Give the preparation type.
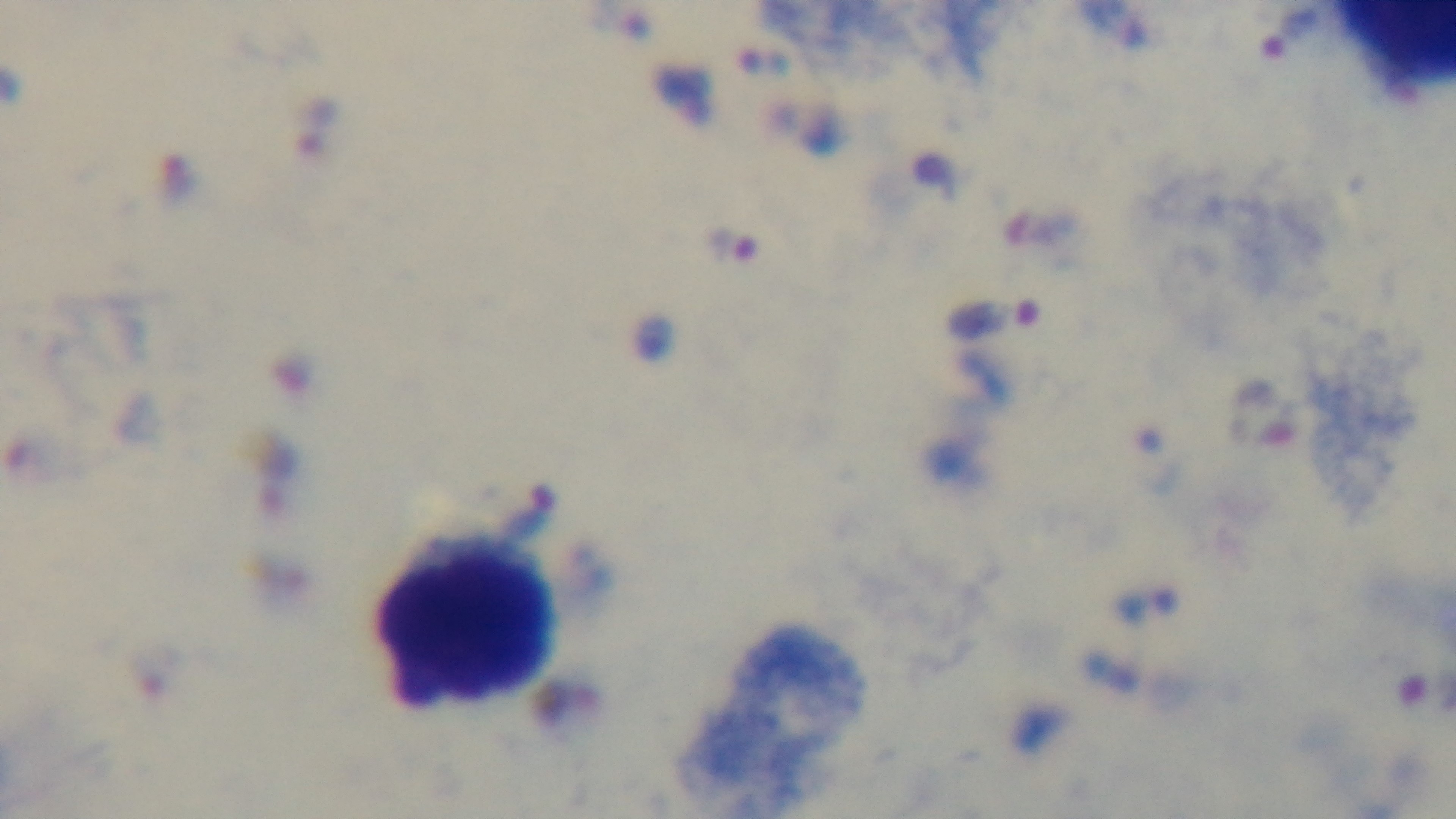

A thick smear.

capture = mounted 4K digital camera
stain = Giemsa
objective = 100x oil immersion
field of view = one from the slide
modality = light microscopy
malaria status = positive